Locate every blood parasite and identify its species.
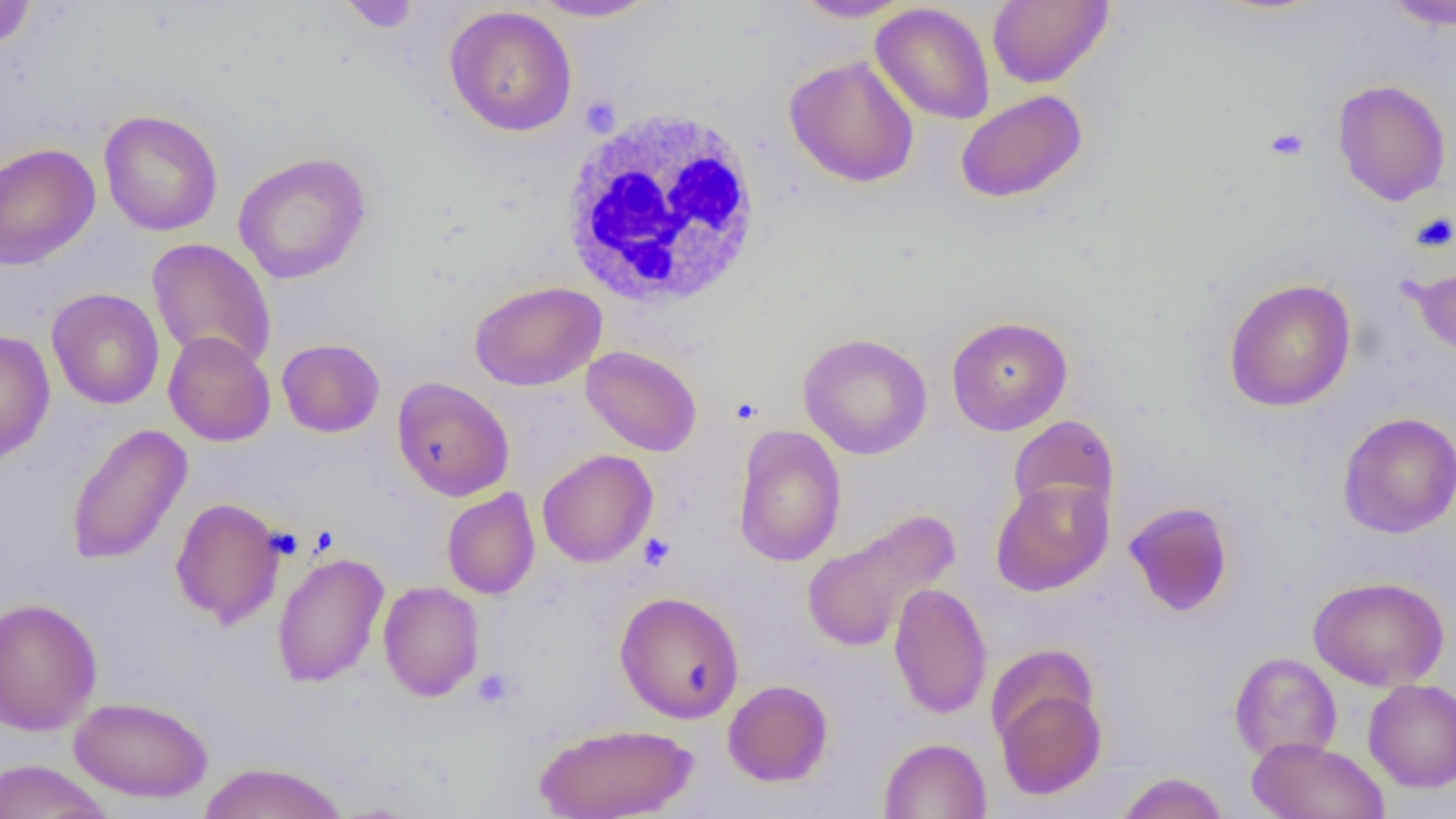
No blood parasites observed.

Approximate bounding boxes as (x1, y1, x2, y2) in pixels. Uninfected red blood cell locations: (337, 0, 423, 33), (987, 0, 1113, 88), (0, 1, 36, 52), (528, 1, 662, 22), (791, 1, 915, 22), (1383, 1, 1456, 31), (871, 2, 995, 125), (444, 5, 577, 137), (785, 56, 920, 188), (1332, 78, 1452, 206), (955, 90, 1087, 204), (99, 109, 223, 237), (0, 142, 101, 269), (232, 151, 372, 284), (147, 238, 277, 371), (1406, 260, 1456, 361), (1223, 278, 1356, 412), (469, 280, 607, 391), (46, 288, 165, 409), (946, 315, 1073, 435), (0, 329, 55, 465), (163, 331, 275, 447), (797, 333, 933, 459), (277, 338, 385, 438), (581, 345, 703, 457), (392, 377, 514, 502), (1338, 412, 1456, 538), (1007, 414, 1120, 523), (65, 423, 191, 566), (732, 425, 847, 567), (537, 449, 658, 568), (991, 479, 1113, 596), (441, 487, 540, 600), (170, 498, 286, 629), (1123, 501, 1234, 617), (801, 508, 961, 654), (271, 552, 389, 687), (1309, 575, 1449, 691), (378, 581, 485, 701), (888, 582, 991, 720), (614, 590, 744, 724), (0, 597, 103, 737), (1229, 652, 1342, 764), (993, 678, 1107, 800), (723, 679, 833, 787), (1363, 679, 1456, 792), (69, 696, 214, 802), (533, 722, 699, 819), (878, 737, 992, 819), (1247, 737, 1390, 819), (0, 759, 114, 819), (196, 761, 349, 818), (1115, 772, 1229, 819). Platelet locations: (1265, 126, 1309, 161), (1410, 213, 1456, 254), (638, 532, 674, 571), (471, 668, 519, 710). White blood cell locations: (557, 107, 766, 311). Slide-level diagnosis: no evidence of blood parasites. Image is 1456×819 pixels. Light microscopy. Thin blood smear. Captured at 1000x magnification. One field of a larger specimen.